Report the malaria status of this cell.
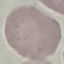
Uninfected.

Summary:
  - Capture: smartphone through the microscope eyepiece
  - Preparation: thin blood smear
  - Stain: Giemsa
  - Image type: automatically extracted cell patch, resized to 64 × 64 pixels